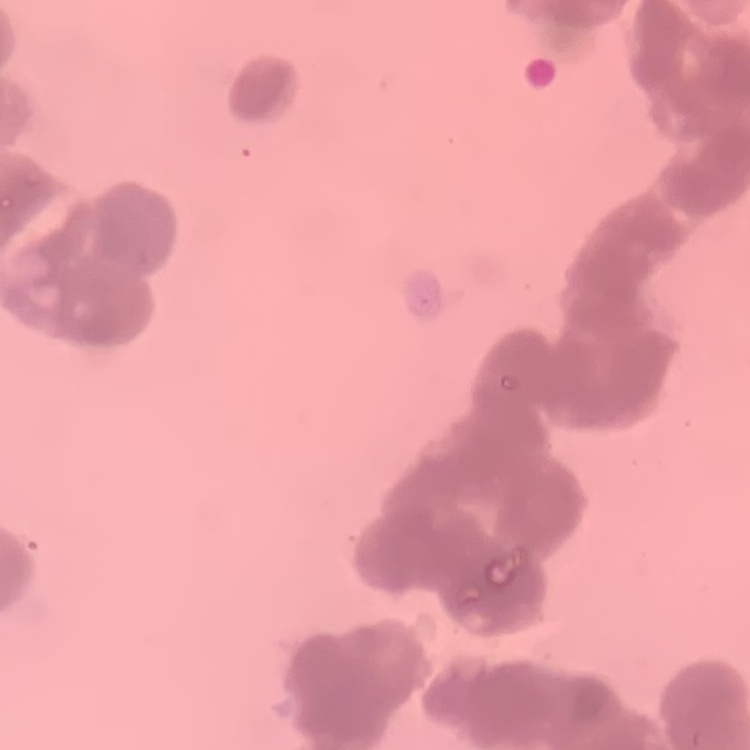
The red blood cells show rouleaux formation. Stained with either Field's or Giemsa. Square crop of a larger photomicrograph. Thin peripheral smear.